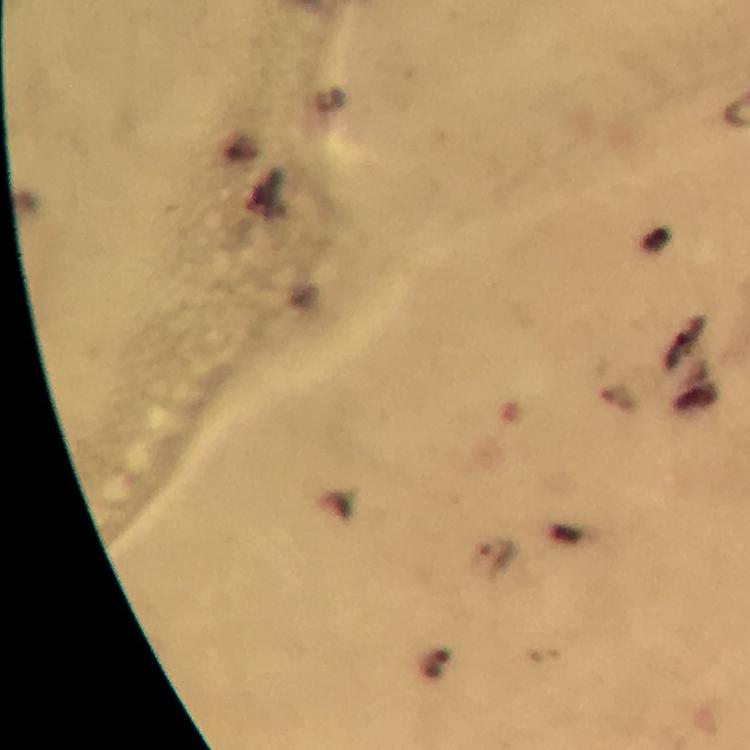

cropped from = a single field of view
Plasmodium parasite locations = approximate centers as {x, y} in pixels: {497, 553}
context = from a malaria diagnostic workup
stain = Giemsa
preparation = thick smear
image size = 750×750 pixels
immersion oil = applied
magnification = 100x
capture = smartphone mounted on the microscope